Describe the morphology of the erythrocytes.
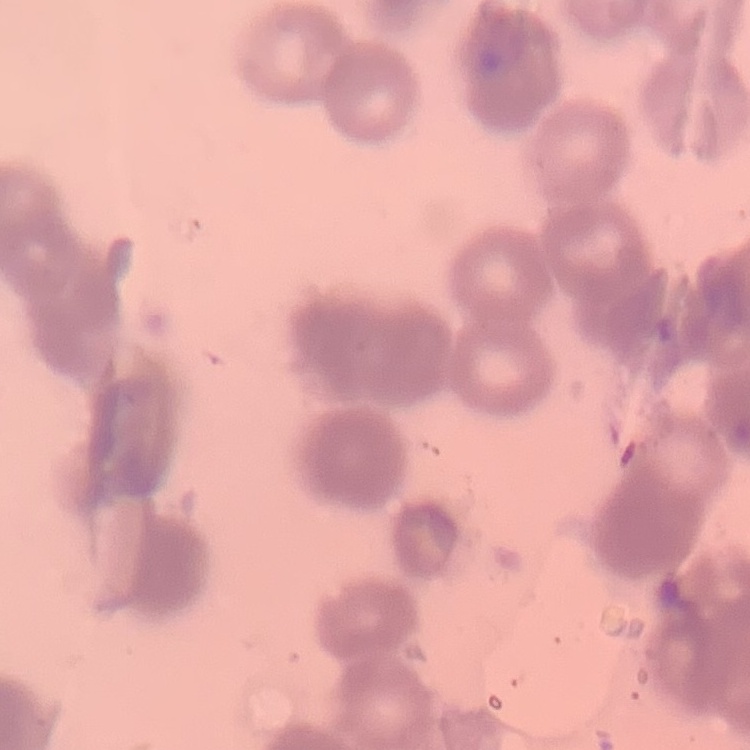
Rouleaux formation.

Summary:
  - Stain: Field's or Giemsa
  - Preparation: thin blood film
  - Image type: one tile cut from a larger photomicrograph